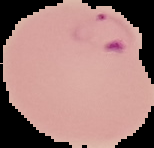
Summary:
  - Result: malaria parasites detected
  - Image type: cell region segmented out of the field of view; surrounding area masked to black
  - Preparation: thin blood film
  - Image size: 154×148 pixels